State the blood parasite species.
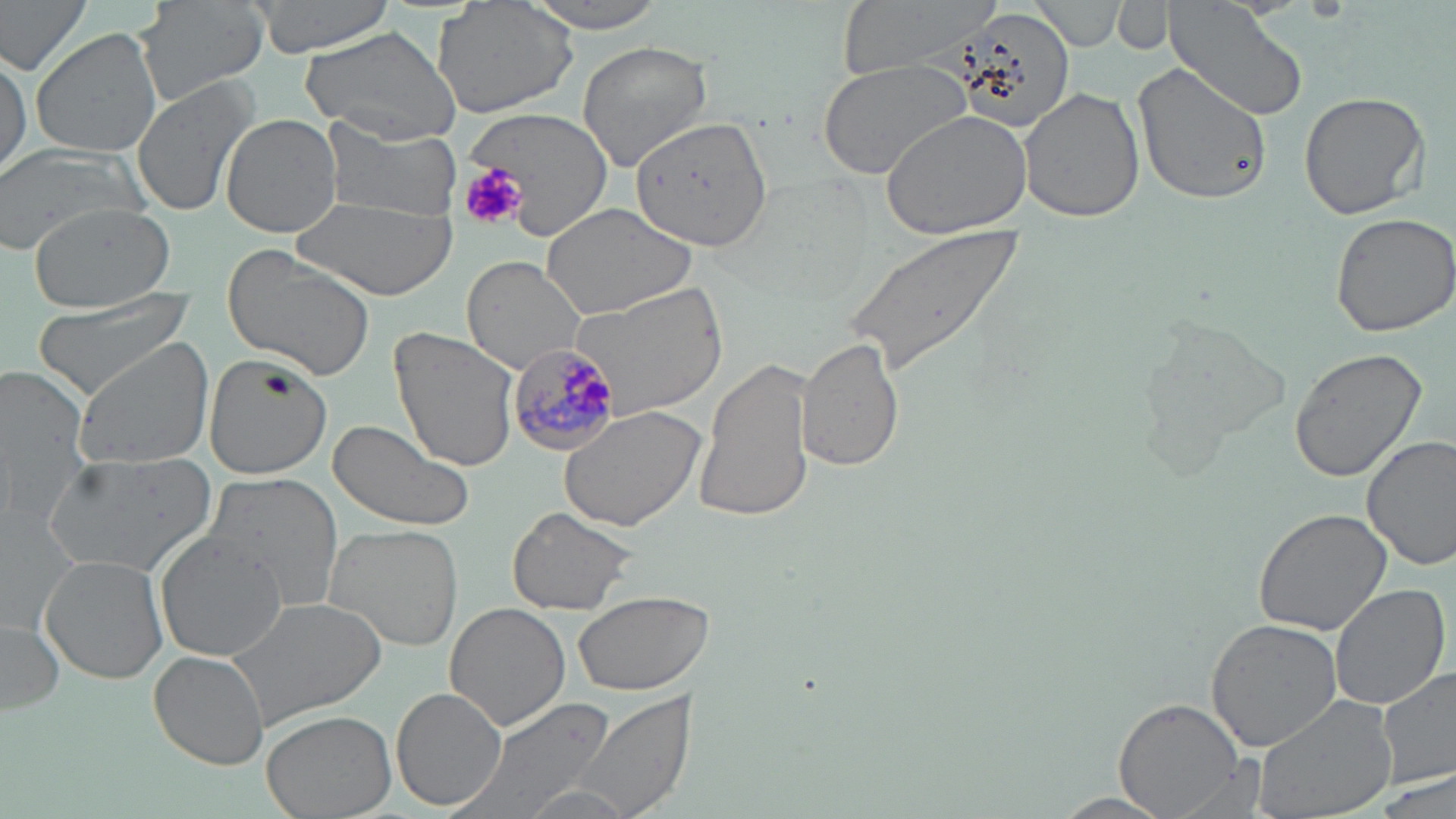
Plasmodium malariae.

Summary:
  - Coordinate format: approximate bounding boxes as named x1/y1/x2/y2 corners in pixels
  - Uninfected red blood cell locations: (x1=0, y1=0, x2=94, y2=79), (x1=137, y1=0, x2=268, y2=104), (x1=244, y1=0, x2=397, y2=58), (x1=432, y1=0, x2=581, y2=120), (x1=516, y1=0, x2=674, y2=32), (x1=832, y1=0, x2=1004, y2=76), (x1=1113, y1=1, x2=1177, y2=55), (x1=1165, y1=1, x2=1309, y2=121), (x1=1032, y1=2, x2=1129, y2=50), (x1=946, y1=12, x2=1086, y2=135), (x1=300, y1=25, x2=460, y2=145), (x1=29, y1=27, x2=163, y2=159), (x1=575, y1=40, x2=711, y2=172), (x1=0, y1=46, x2=30, y2=178), (x1=815, y1=58, x2=975, y2=181), (x1=1134, y1=61, x2=1272, y2=208), (x1=130, y1=76, x2=260, y2=218), (x1=1019, y1=86, x2=1145, y2=223), (x1=1300, y1=92, x2=1428, y2=220), (x1=462, y1=107, x2=615, y2=240), (x1=880, y1=109, x2=1031, y2=242), (x1=222, y1=114, x2=343, y2=240), (x1=321, y1=116, x2=463, y2=222), (x1=631, y1=118, x2=773, y2=251), (x1=0, y1=150, x2=152, y2=252), (x1=296, y1=196, x2=458, y2=302), (x1=26, y1=201, x2=176, y2=312), (x1=541, y1=201, x2=699, y2=318), (x1=1328, y1=210, x2=1456, y2=336), (x1=839, y1=224, x2=1025, y2=380), (x1=221, y1=247, x2=379, y2=380), (x1=460, y1=256, x2=587, y2=374), (x1=570, y1=281, x2=729, y2=418), (x1=29, y1=289, x2=198, y2=400), (x1=1136, y1=313, x2=1287, y2=463), (x1=388, y1=326, x2=521, y2=475), (x1=798, y1=335, x2=903, y2=473), (x1=73, y1=341, x2=214, y2=471), (x1=1289, y1=347, x2=1427, y2=483), (x1=202, y1=354, x2=334, y2=477), (x1=695, y1=354, x2=818, y2=525), (x1=0, y1=361, x2=94, y2=523), (x1=558, y1=404, x2=704, y2=532), (x1=327, y1=419, x2=477, y2=534), (x1=1362, y1=435, x2=1456, y2=572), (x1=44, y1=450, x2=218, y2=578), (x1=199, y1=470, x2=347, y2=617), (x1=507, y1=505, x2=640, y2=617), (x1=1253, y1=507, x2=1392, y2=635), (x1=324, y1=522, x2=464, y2=651), (x1=156, y1=533, x2=291, y2=660), (x1=40, y1=553, x2=170, y2=684), (x1=1329, y1=583, x2=1451, y2=714), (x1=571, y1=589, x2=714, y2=693), (x1=223, y1=594, x2=388, y2=728), (x1=443, y1=602, x2=570, y2=732), (x1=1205, y1=618, x2=1341, y2=753), (x1=2, y1=619, x2=63, y2=717), (x1=149, y1=651, x2=268, y2=767), (x1=1377, y1=667, x2=1456, y2=791), (x1=392, y1=688, x2=506, y2=810), (x1=568, y1=688, x2=698, y2=819), (x1=1251, y1=694, x2=1398, y2=819), (x1=451, y1=697, x2=618, y2=819), (x1=1113, y1=697, x2=1247, y2=818), (x1=261, y1=709, x2=397, y2=819), (x1=1166, y1=756, x2=1274, y2=819), (x1=1377, y1=767, x2=1455, y2=819), (x1=1051, y1=793, x2=1174, y2=818)
  - Plasmodium malariae-infected red blood cell locations: (x1=507, y1=342, x2=629, y2=454)
  - Platelet locations: (x1=457, y1=165, x2=528, y2=230)
  - Preparation: thin blood film
  - Modality: light microscopy
  - Field of view: single
  - Image size: 1456×819 pixels
  - Magnification: 1000x
  - Stain: May-Grünwald-Giemsa